State which parasite is depicted.
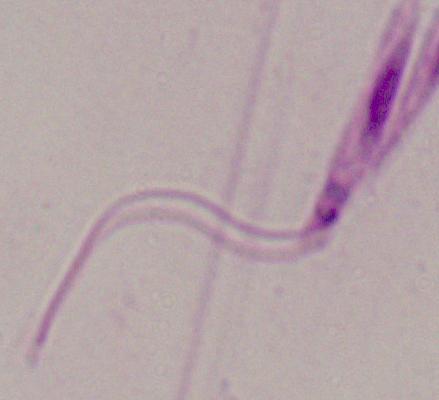

This is Leishmania.

Summary:
  - Modality: micrograph
  - Magnification: 1000x